Assess this cell for malaria.
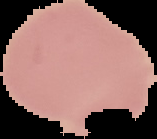

It is uninfected.

image_size: 157×139 pixels
image_type: segmented cell region on a black background
preparation: thin blood smear